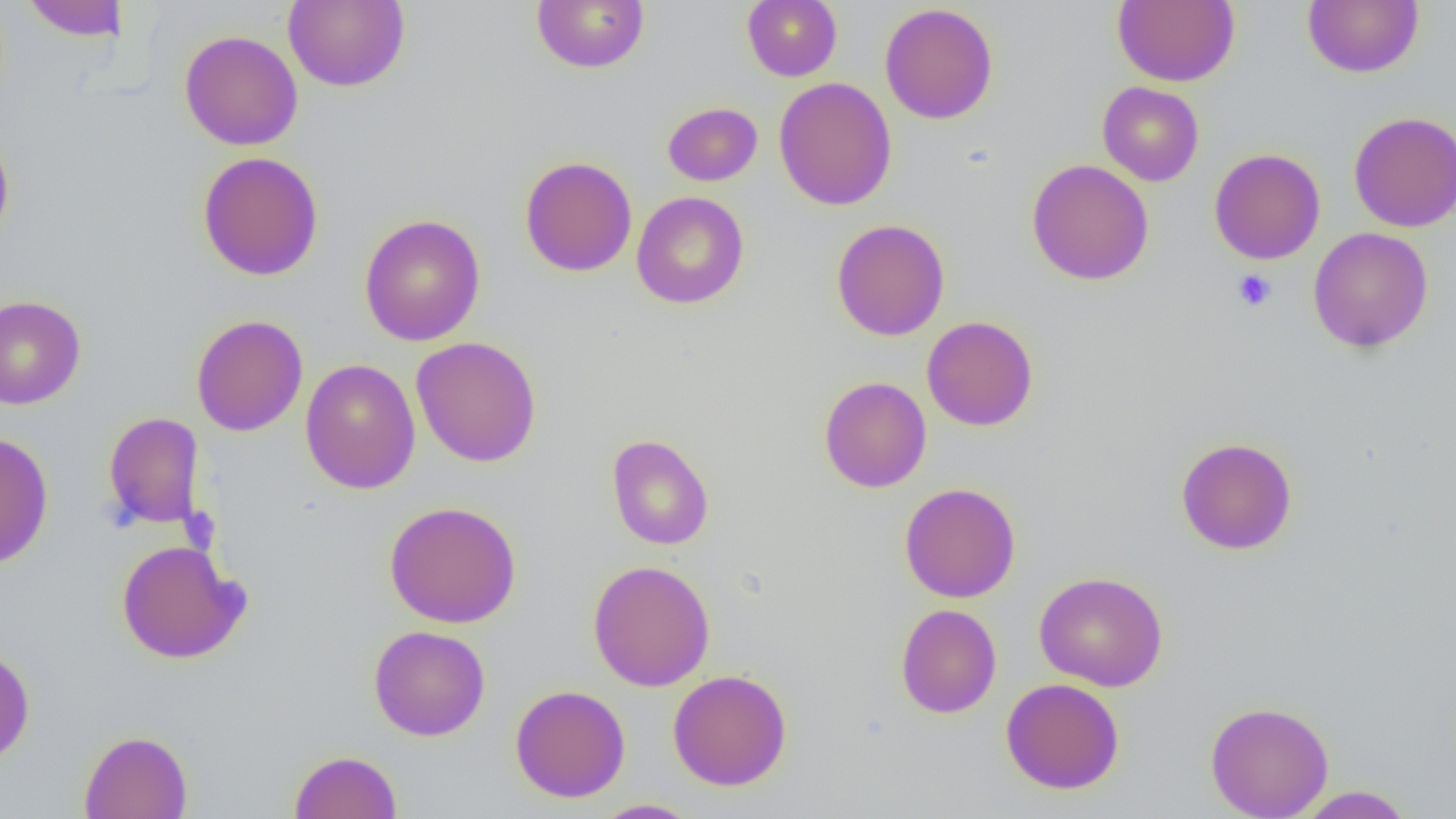
slide-level diagnosis = no evidence of blood parasites
preparation = thin blood film
uninfected red blood cell locations = approximate bounding boxes as (x1, y1, x2, y2) in pixels: (20, 0, 130, 41), (283, 0, 410, 92), (531, 0, 649, 74), (742, 0, 842, 81), (1111, 0, 1240, 87), (1302, 0, 1424, 78), (879, 3, 998, 125), (178, 30, 304, 151), (773, 77, 897, 211), (1097, 81, 1204, 186), (662, 102, 763, 186), (1349, 111, 1456, 232), (0, 130, 15, 248), (1209, 148, 1326, 264), (197, 151, 324, 281), (520, 156, 637, 277), (1027, 159, 1154, 285), (631, 190, 749, 309), (359, 214, 485, 346), (831, 219, 950, 341), (1308, 227, 1433, 353), (0, 295, 86, 410), (190, 314, 308, 436), (922, 316, 1038, 431), (410, 336, 542, 467), (300, 358, 421, 494), (818, 376, 931, 493), (103, 411, 204, 530), (0, 431, 54, 570), (606, 434, 714, 550), (1176, 437, 1297, 554), (899, 482, 1021, 603), (384, 501, 522, 628), (116, 539, 249, 664), (587, 560, 716, 691), (1034, 571, 1168, 691), (895, 604, 1001, 718), (368, 625, 490, 741), (0, 645, 35, 765), (667, 669, 792, 791), (1000, 678, 1126, 795), (510, 685, 630, 803), (1205, 700, 1334, 819), (79, 729, 193, 819), (288, 750, 403, 818), (1295, 786, 1415, 818), (590, 799, 700, 818)
image size = 1456×819 pixels
magnification = 1000x
platelet locations = approximate bounding boxes as (x1, y1, x2, y2) in pixels: (1232, 269, 1278, 312)
modality = optical microscopy
field of view = single